Classify the preparation.
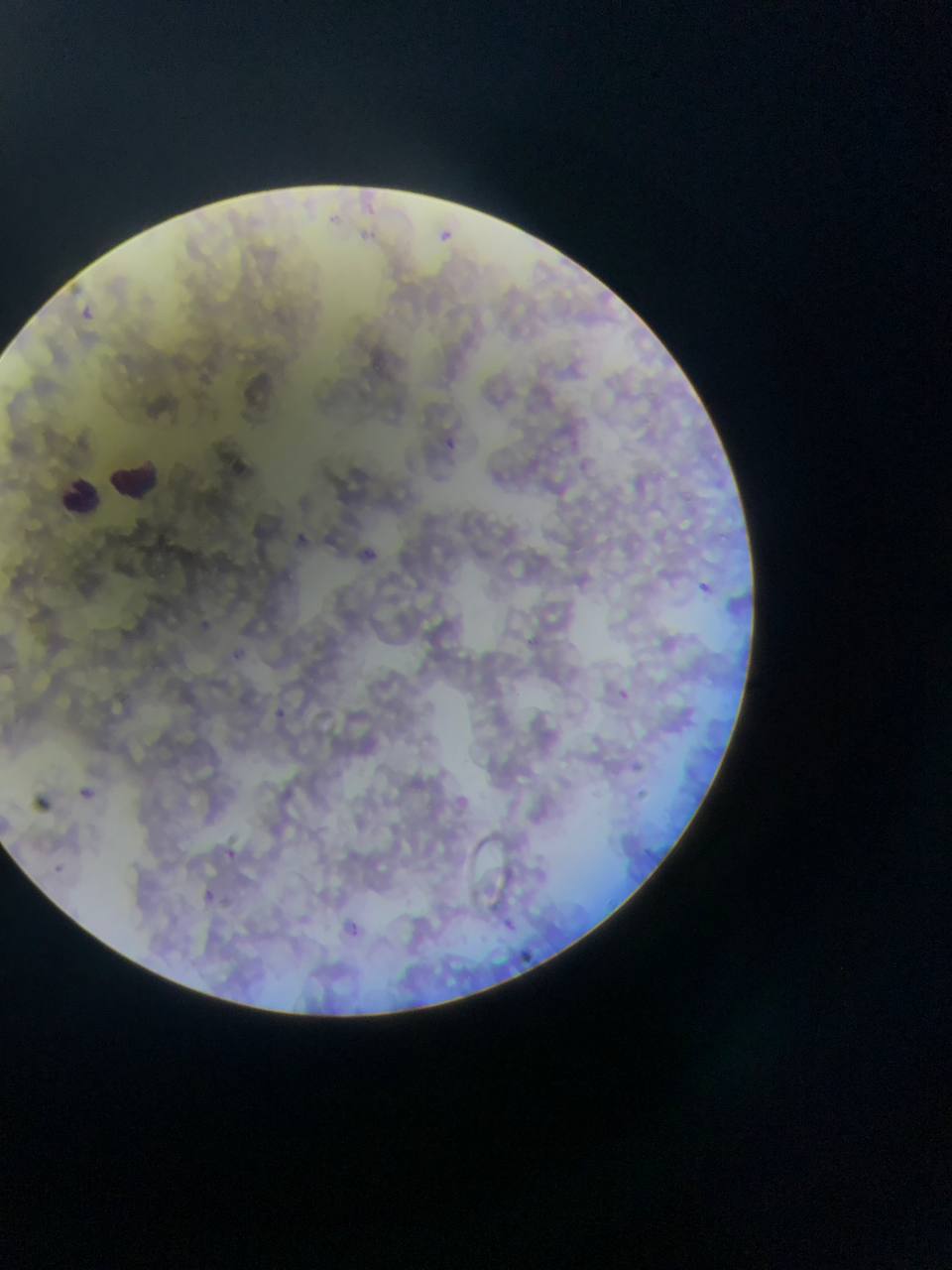

Thin blood film.

Approximate bounding boxes as {left, top, right, bottom} in pixels. Leukocyte locations: {110, 459, 157, 506}, {61, 472, 107, 511}. Malaria parasite locations: {437, 225, 457, 247}, {83, 305, 96, 318}, {438, 435, 463, 455}, {301, 530, 324, 555}, {358, 542, 387, 569}, {695, 578, 722, 601}, {196, 618, 218, 634}, {608, 684, 640, 707}, {267, 704, 304, 724}, {625, 762, 652, 778}, {78, 783, 98, 805}, {216, 840, 254, 865}, {195, 887, 220, 909}, {499, 913, 516, 934}, {341, 916, 366, 933}, {516, 942, 535, 968}. One field of view. Mobile-phone photograph taken through the microscope. Collected in Ghana. Image is 952×1270 pixels.